Give the extent of all Plasmodium malariae-infected red blood cells.
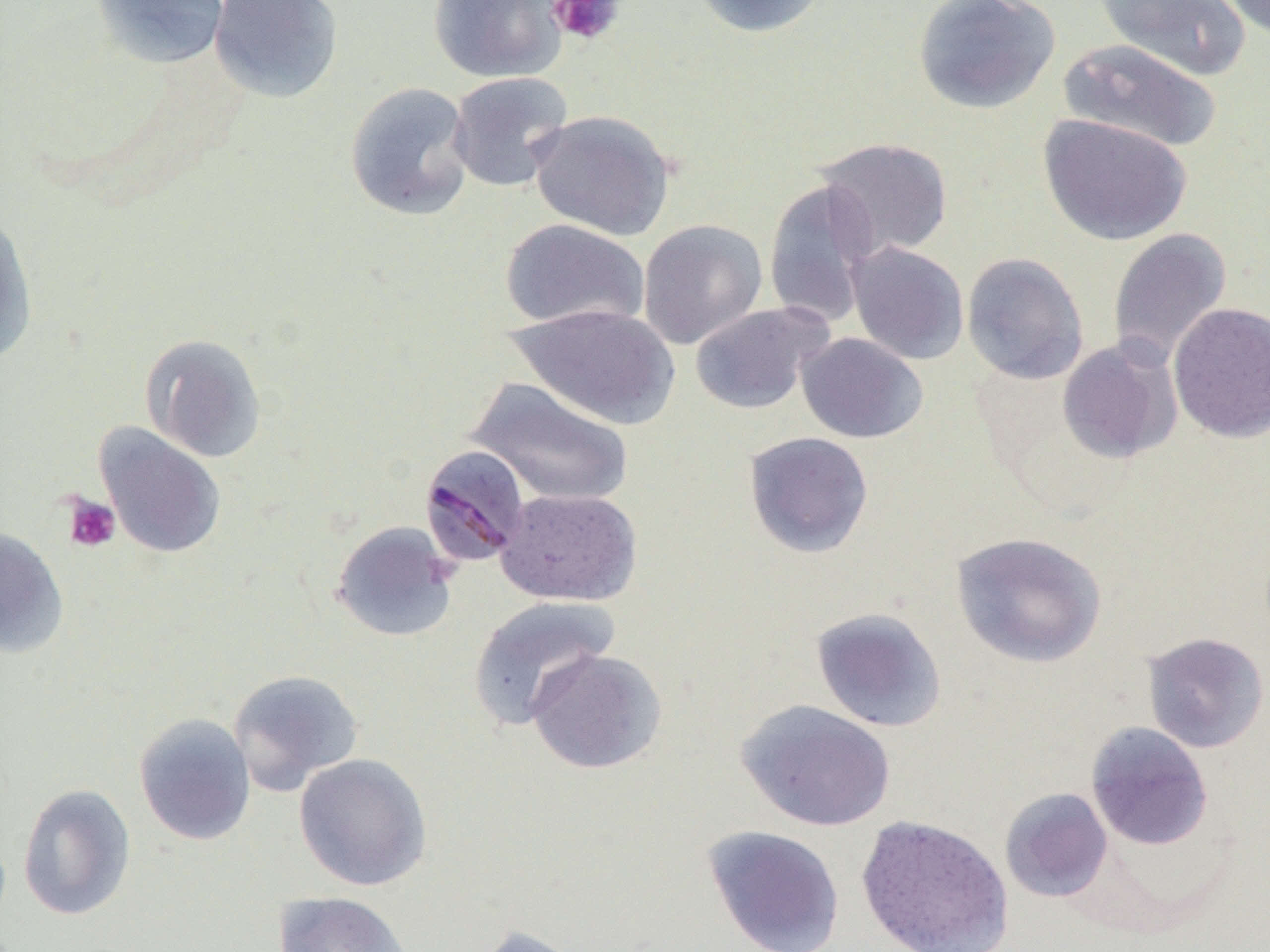
Approximate bounding boxes as named x1/y1/x2/y2 corners in pixels.
Plasmodium malariae-infected red blood cells: (x1=419, y1=444, x2=529, y2=567).

Platelet locations: (x1=547, y1=0, x2=625, y2=47), (x1=63, y1=494, x2=121, y2=552). Uninfected red blood cell locations: (x1=91, y1=0, x2=231, y2=69), (x1=208, y1=0, x2=344, y2=104), (x1=428, y1=0, x2=567, y2=83), (x1=687, y1=0, x2=834, y2=39), (x1=912, y1=0, x2=1061, y2=114), (x1=1093, y1=0, x2=1251, y2=82), (x1=1216, y1=0, x2=1269, y2=41), (x1=1057, y1=39, x2=1224, y2=154), (x1=446, y1=72, x2=574, y2=193), (x1=345, y1=82, x2=475, y2=221), (x1=527, y1=109, x2=674, y2=240), (x1=1038, y1=113, x2=1193, y2=246), (x1=813, y1=137, x2=954, y2=262), (x1=763, y1=179, x2=880, y2=328), (x1=0, y1=208, x2=38, y2=368), (x1=500, y1=218, x2=649, y2=331), (x1=638, y1=219, x2=768, y2=349), (x1=1107, y1=227, x2=1232, y2=368), (x1=846, y1=241, x2=969, y2=365), (x1=961, y1=252, x2=1089, y2=385), (x1=689, y1=301, x2=831, y2=414), (x1=1168, y1=302, x2=1270, y2=443), (x1=508, y1=303, x2=680, y2=429), (x1=796, y1=332, x2=928, y2=443), (x1=139, y1=333, x2=267, y2=463), (x1=1056, y1=339, x2=1182, y2=464), (x1=465, y1=376, x2=634, y2=508), (x1=94, y1=424, x2=226, y2=559), (x1=743, y1=431, x2=874, y2=559), (x1=496, y1=487, x2=641, y2=606), (x1=331, y1=521, x2=460, y2=643), (x1=0, y1=526, x2=69, y2=658), (x1=950, y1=531, x2=1107, y2=668), (x1=467, y1=594, x2=620, y2=730), (x1=811, y1=607, x2=947, y2=733), (x1=1142, y1=632, x2=1269, y2=753), (x1=526, y1=648, x2=667, y2=774), (x1=227, y1=669, x2=365, y2=796), (x1=736, y1=699, x2=896, y2=832), (x1=133, y1=712, x2=256, y2=846), (x1=1085, y1=722, x2=1213, y2=851), (x1=293, y1=752, x2=433, y2=891), (x1=17, y1=783, x2=136, y2=921), (x1=999, y1=787, x2=1113, y2=903), (x1=854, y1=814, x2=1014, y2=952), (x1=702, y1=824, x2=845, y2=952), (x1=272, y1=891, x2=414, y2=952), (x1=473, y1=924, x2=585, y2=952). Slide-level diagnosis: Plasmodium malariae. Image is 1270×952 pixels. Thin blood smear. Light microscopy. Single field of view. Captured at 1000x magnification.